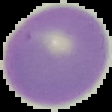
Summary:
  - Image size: 112×112 pixels
  - Image type: segmented cell region on a black background
  - Preparation: thin blood smear
  - Result: no malaria parasites detected